Classify this cell by malaria status.
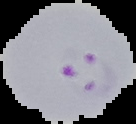

Parasitized.

Summary:
  - Image type: cell region segmented out of the field of view; surrounding area masked to black
  - Image size: 136×124 pixels
  - Preparation: thin blood smear